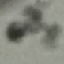

result = no malaria parasites seen
capture = smartphone camera at the microscope eyepiece
image type = automatically extracted cell patch, resized to 64 × 64 pixels
stain = Giemsa
preparation = thin blood film